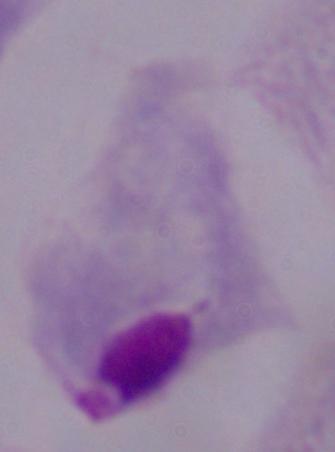
magnification = 1000x
modality = photomicrograph
identification = trichomonad